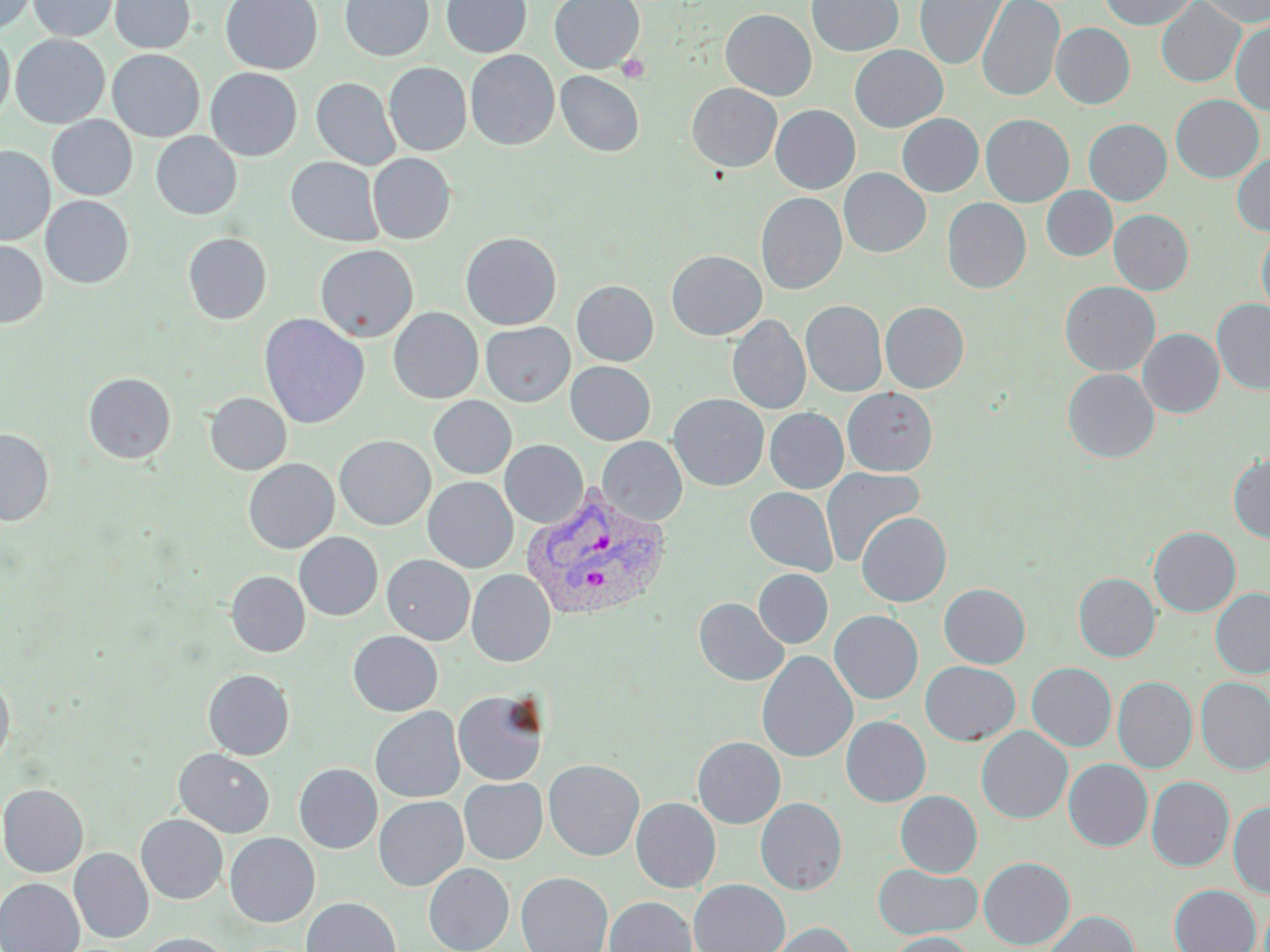
Approximate bounding boxes as (x1,y1)-(x2,y2) corner pairs in pixels. Plasmodium vivax-infected red blood cell locations: (521,486)-(670,622). Uninfected red blood cell locations: (0,0)-(37,33), (28,0)-(118,41), (109,0)-(195,53), (221,0)-(323,74), (340,0)-(433,61), (441,0)-(532,58), (549,0)-(645,73), (807,0)-(904,57), (915,0)-(1009,69), (977,0)-(1064,102), (1099,0)-(1197,30), (1197,0)-(1270,27), (1156,1)-(1245,87), (720,9)-(816,100), (1231,21)-(1270,116), (1051,23)-(1135,109), (0,30)-(14,124), (11,34)-(109,128), (850,45)-(948,132), (107,49)-(204,142), (465,50)-(559,150), (385,62)-(471,155), (205,68)-(302,160), (555,71)-(644,157), (312,78)-(400,170), (687,83)-(782,172), (1170,94)-(1263,183), (771,105)-(860,194), (897,113)-(984,196), (980,114)-(1074,207), (47,115)-(137,200), (1084,119)-(1171,205), (151,132)-(242,219), (0,145)-(54,245), (1232,152)-(1270,236), (368,153)-(456,244), (286,157)-(384,246), (839,168)-(931,258), (1041,186)-(1117,261), (756,192)-(847,295), (41,196)-(134,288), (942,198)-(1031,293), (1109,209)-(1193,295), (1256,228)-(1270,319), (461,232)-(562,330), (183,233)-(272,324), (0,240)-(48,328), (315,244)-(419,341), (666,250)-(766,340), (571,280)-(659,366), (1059,281)-(1160,376), (1212,299)-(1270,395), (801,300)-(887,397), (880,301)-(969,393), (388,308)-(483,403), (259,313)-(369,429), (727,315)-(811,414), (481,322)-(575,406), (1138,328)-(1224,417), (565,361)-(655,445), (1062,368)-(1159,462), (83,372)-(176,463), (843,388)-(937,475), (205,393)-(291,475), (668,393)-(769,490), (428,396)-(517,479), (765,408)-(848,493), (0,428)-(54,525), (335,435)-(436,530), (597,436)-(687,526), (500,440)-(588,528), (243,450)-(437,542), (1229,454)-(1270,542), (243,458)-(339,553), (820,467)-(925,567), (423,477)-(518,572), (745,487)-(838,575), (856,512)-(951,606), (1149,527)-(1240,617), (294,532)-(383,620), (382,554)-(475,645), (467,569)-(556,666), (753,569)-(832,648), (226,571)-(310,656), (1074,573)-(1160,662), (939,583)-(1030,668), (1210,587)-(1270,679), (693,597)-(789,686), (829,610)-(923,704), (348,631)-(442,716), (756,651)-(857,763), (920,661)-(1021,745), (1027,663)-(1116,751), (203,669)-(294,759), (0,670)-(14,769), (1113,677)-(1196,773), (1196,677)-(1270,774), (453,689)-(549,785), (370,707)-(465,803), (841,716)-(930,807), (976,726)-(1073,823), (693,736)-(785,828), (174,749)-(274,837), (544,759)-(644,860), (1064,759)-(1152,851), (294,763)-(382,853), (1147,776)-(1234,871), (459,777)-(547,864), (0,783)-(88,876), (896,790)-(982,877), (374,796)-(468,891), (631,797)-(721,892), (755,797)-(847,895), (1229,801)-(1270,898), (136,814)-(227,904), (225,833)-(320,927), (69,848)-(153,943), (979,856)-(1075,949), (423,863)-(514,952), (873,864)-(982,939), (516,871)-(612,952), (0,878)-(84,952), (689,879)-(790,952), (1169,884)-(1261,952), (604,896)-(696,952), (301,898)-(401,952), (1044,910)-(1140,952), (763,922)-(857,952), (136,932)-(233,952), (884,932)-(976,952). Platelet locations: (617,53)-(651,83). Slide-level diagnosis: Plasmodium vivax. Single field of view. May-Grünwald-Giemsa stain. Captured at 1000x magnification. Thin blood smear. Optical microscopy. Image is 1270×952 pixels.